Locate and identify every blood parasite.
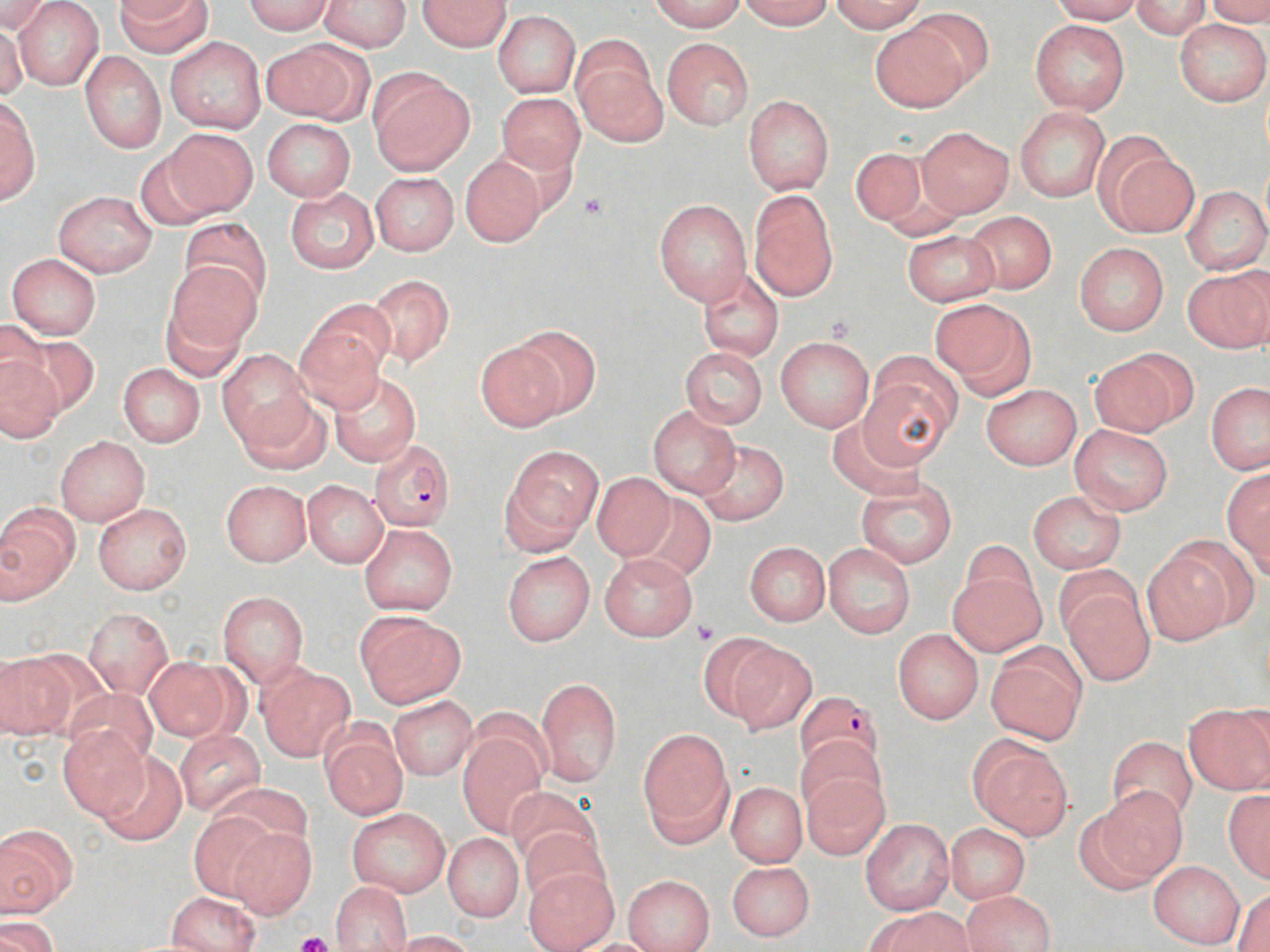
Approximate bounding boxes as named x1/y1/x2/y2 corners in pixels.
Plasmodium falciparum-infected red blood cells: (x1=369, y1=437, x2=456, y2=531), (x1=794, y1=689, x2=884, y2=774).
No Plasmodium ovale, Plasmodium malariae, Plasmodium vivax, Babesia divergens, or Trypanosoma brucei observed.

Summary:
  - Uninfected red blood cell locations: (x1=0, y1=0, x2=34, y2=67), (x1=115, y1=0, x2=211, y2=58), (x1=318, y1=0, x2=412, y2=52), (x1=418, y1=0, x2=511, y2=52), (x1=652, y1=0, x2=745, y2=32), (x1=739, y1=0, x2=833, y2=29), (x1=828, y1=0, x2=929, y2=33), (x1=1050, y1=0, x2=1143, y2=24), (x1=1206, y1=0, x2=1270, y2=26), (x1=0, y1=1, x2=55, y2=35), (x1=240, y1=1, x2=335, y2=34), (x1=1130, y1=1, x2=1212, y2=39), (x1=13, y1=2, x2=104, y2=89), (x1=902, y1=7, x2=995, y2=93), (x1=493, y1=11, x2=580, y2=96), (x1=1030, y1=19, x2=1130, y2=115), (x1=1175, y1=19, x2=1270, y2=106), (x1=869, y1=21, x2=972, y2=114), (x1=0, y1=22, x2=26, y2=101), (x1=166, y1=37, x2=267, y2=133), (x1=663, y1=38, x2=754, y2=130), (x1=263, y1=39, x2=371, y2=124), (x1=573, y1=41, x2=665, y2=144), (x1=80, y1=52, x2=167, y2=153), (x1=369, y1=70, x2=473, y2=176), (x1=496, y1=92, x2=585, y2=175), (x1=743, y1=95, x2=834, y2=194), (x1=0, y1=97, x2=41, y2=205), (x1=1014, y1=108, x2=1110, y2=202), (x1=261, y1=119, x2=355, y2=202), (x1=916, y1=126, x2=1013, y2=217), (x1=166, y1=128, x2=258, y2=217), (x1=1100, y1=145, x2=1199, y2=238), (x1=850, y1=146, x2=934, y2=230), (x1=135, y1=147, x2=227, y2=231), (x1=460, y1=154, x2=546, y2=247), (x1=370, y1=172, x2=458, y2=256), (x1=1182, y1=185, x2=1269, y2=276), (x1=284, y1=187, x2=377, y2=275), (x1=53, y1=190, x2=158, y2=276), (x1=748, y1=191, x2=839, y2=301), (x1=654, y1=199, x2=750, y2=305), (x1=962, y1=211, x2=1057, y2=292), (x1=177, y1=215, x2=273, y2=307), (x1=902, y1=230, x2=1000, y2=306), (x1=1074, y1=242, x2=1169, y2=335), (x1=6, y1=253, x2=101, y2=339), (x1=164, y1=262, x2=260, y2=355), (x1=696, y1=267, x2=785, y2=362), (x1=1184, y1=267, x2=1270, y2=353), (x1=366, y1=275, x2=454, y2=366), (x1=930, y1=299, x2=1036, y2=397), (x1=159, y1=301, x2=247, y2=382), (x1=295, y1=309, x2=391, y2=409), (x1=0, y1=319, x2=51, y2=401), (x1=507, y1=324, x2=599, y2=418), (x1=9, y1=328, x2=96, y2=414), (x1=775, y1=335, x2=875, y2=432), (x1=474, y1=339, x2=569, y2=431), (x1=680, y1=347, x2=767, y2=429), (x1=218, y1=350, x2=313, y2=447), (x1=1088, y1=350, x2=1192, y2=437), (x1=0, y1=358, x2=63, y2=441), (x1=859, y1=359, x2=959, y2=466), (x1=118, y1=363, x2=205, y2=447), (x1=328, y1=369, x2=423, y2=468), (x1=1206, y1=382, x2=1270, y2=474), (x1=982, y1=384, x2=1082, y2=470), (x1=234, y1=394, x2=331, y2=475), (x1=647, y1=406, x2=741, y2=496), (x1=827, y1=418, x2=927, y2=500), (x1=1069, y1=423, x2=1173, y2=515), (x1=55, y1=436, x2=149, y2=525), (x1=694, y1=439, x2=790, y2=525), (x1=503, y1=448, x2=600, y2=550), (x1=1223, y1=470, x2=1270, y2=571), (x1=592, y1=471, x2=676, y2=562), (x1=855, y1=477, x2=958, y2=568), (x1=221, y1=480, x2=311, y2=567), (x1=303, y1=481, x2=387, y2=568), (x1=1027, y1=491, x2=1126, y2=573), (x1=630, y1=493, x2=717, y2=581), (x1=93, y1=502, x2=192, y2=596), (x1=0, y1=508, x2=78, y2=601), (x1=360, y1=523, x2=458, y2=615), (x1=960, y1=539, x2=1038, y2=618), (x1=744, y1=542, x2=829, y2=625), (x1=823, y1=544, x2=915, y2=638), (x1=1142, y1=544, x2=1239, y2=644), (x1=502, y1=551, x2=594, y2=646), (x1=600, y1=554, x2=696, y2=641), (x1=948, y1=569, x2=1045, y2=657), (x1=1059, y1=576, x2=1155, y2=688), (x1=217, y1=591, x2=309, y2=687), (x1=84, y1=608, x2=172, y2=698), (x1=356, y1=613, x2=466, y2=708), (x1=892, y1=628, x2=983, y2=724), (x1=696, y1=631, x2=784, y2=723), (x1=727, y1=642, x2=817, y2=734), (x1=986, y1=643, x2=1089, y2=745), (x1=0, y1=653, x2=74, y2=740), (x1=143, y1=657, x2=242, y2=742), (x1=256, y1=664, x2=355, y2=762), (x1=536, y1=676, x2=622, y2=786), (x1=63, y1=687, x2=159, y2=770), (x1=388, y1=695, x2=477, y2=780), (x1=1183, y1=704, x2=1270, y2=794), (x1=56, y1=726, x2=148, y2=820), (x1=320, y1=726, x2=408, y2=820), (x1=175, y1=729, x2=265, y2=815), (x1=639, y1=729, x2=734, y2=845), (x1=457, y1=730, x2=548, y2=836), (x1=797, y1=736, x2=887, y2=823), (x1=1106, y1=736, x2=1197, y2=824), (x1=970, y1=737, x2=1073, y2=841), (x1=95, y1=750, x2=186, y2=846), (x1=799, y1=768, x2=890, y2=859), (x1=727, y1=782, x2=806, y2=866), (x1=504, y1=786, x2=599, y2=871), (x1=1087, y1=786, x2=1187, y2=884), (x1=1223, y1=790, x2=1270, y2=881), (x1=347, y1=807, x2=450, y2=897), (x1=186, y1=810, x2=277, y2=902), (x1=861, y1=818, x2=953, y2=916), (x1=944, y1=823, x2=1030, y2=905), (x1=0, y1=824, x2=76, y2=917), (x1=520, y1=826, x2=611, y2=909), (x1=228, y1=827, x2=320, y2=916), (x1=443, y1=833, x2=523, y2=923), (x1=1147, y1=860, x2=1245, y2=949), (x1=726, y1=861, x2=815, y2=941), (x1=523, y1=865, x2=618, y2=951), (x1=623, y1=875, x2=715, y2=952), (x1=330, y1=883, x2=412, y2=951), (x1=1232, y1=886, x2=1270, y2=950), (x1=962, y1=890, x2=1055, y2=952), (x1=168, y1=892, x2=260, y2=952), (x1=869, y1=907, x2=972, y2=952), (x1=3, y1=918, x2=58, y2=952), (x1=391, y1=930, x2=479, y2=952), (x1=567, y1=938, x2=671, y2=951)
  - Platelet locations: (x1=578, y1=191, x2=608, y2=220), (x1=692, y1=619, x2=720, y2=645), (x1=294, y1=931, x2=333, y2=952)
  - Slide-level diagnosis: Plasmodium falciparum
  - Modality: optical microscopy
  - Stain: May-Grünwald-Giemsa
  - Magnification: 1000x
  - Preparation: thin blood film
  - Field of view: single
  - Image size: 1270×952 pixels